Classify this cell by malaria status.
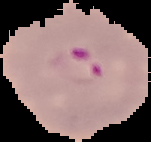
It is parasitized.

Summary:
  - Preparation: thin blood film
  - Image type: segmented cell region on a black background
  - Image size: 151×142 pixels